Locate every leukocyte (white blood cell).
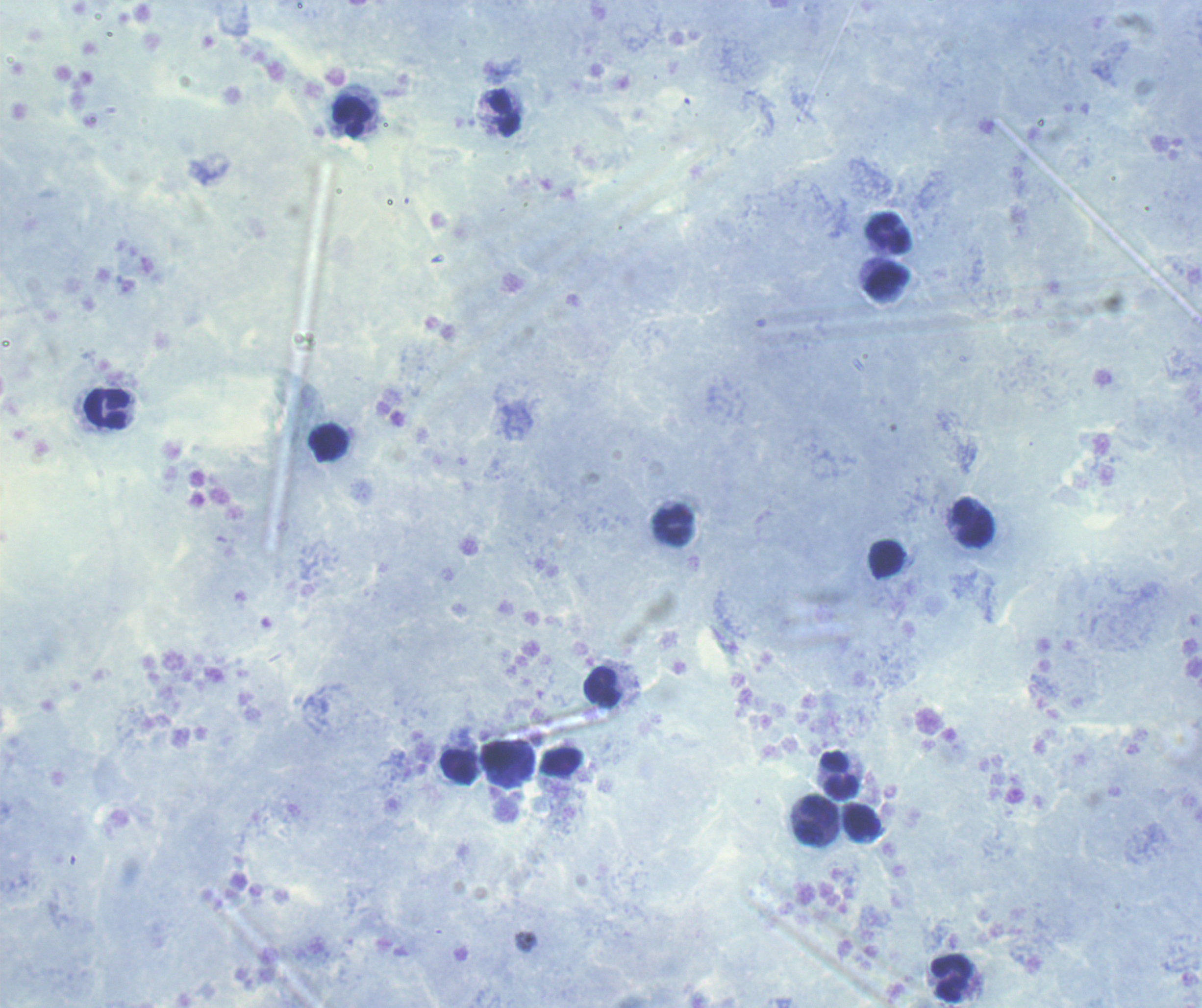

Approximate centers as (x, y) in pixels.
Leukocytes: (504, 114), (351, 116), (888, 234), (887, 280), (107, 408), (328, 442), (973, 523), (673, 524), (887, 559), (602, 687), (508, 760), (459, 768), (840, 775), (816, 821), (861, 822), (951, 979).

Coloration quality: good. Thick blood smear. Romanowsky stain. Result: no Plasmodium parasites detected. Captured at 100x magnification. Background quality: satisfactory. Previously used in a real diagnosis. Single field of view. Image is 1202×1008 pixels.